Locate every leukocyte (white blood cell).
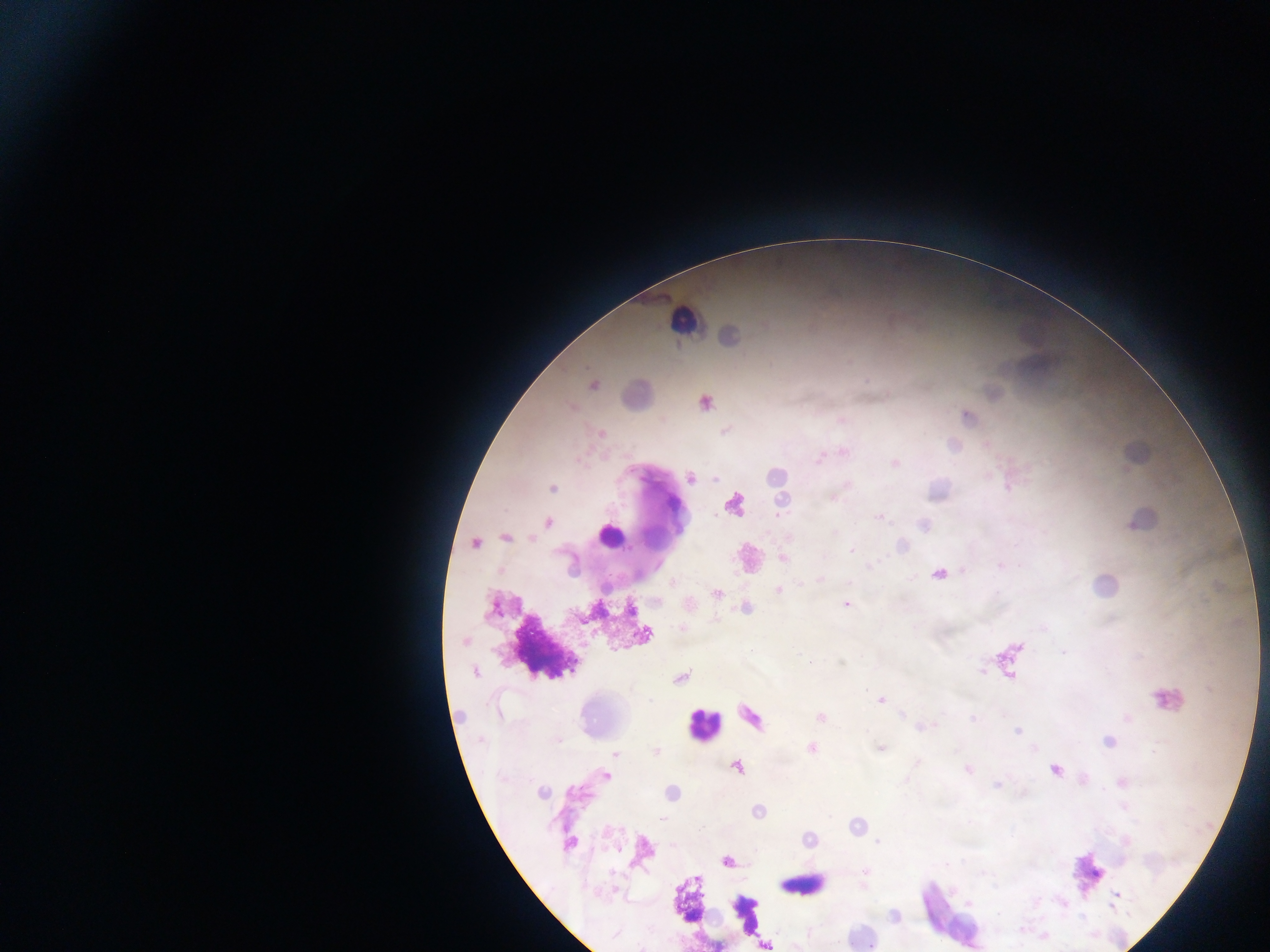
Approximate centers as [x, y] in pixels.
Leukocytes: [681, 320], [609, 536], [657, 537], [702, 725], [800, 887].

image size = 1270×952 pixels
capture = mobile-phone photograph through a microscope
country = Ghana
field of view = single
preparation = thick blood film
Plasmodium parasite locations = approximate centers as [x, y] in pixels: [593, 385], [705, 403], [967, 416], [601, 433], [690, 478], [553, 488], [879, 517], [547, 522], [505, 538], [475, 544], [851, 551], [782, 558], [939, 575], [779, 590], [716, 595], [846, 604], [631, 610], [682, 628], [465, 641], [475, 672], [680, 677], [650, 700], [880, 700], [821, 717], [973, 718], [1017, 731], [812, 749], [656, 751], [616, 753], [736, 768], [968, 769], [1054, 770], [606, 776], [541, 793], [662, 819], [877, 842], [569, 843], [726, 861], [1116, 894], [1111, 906]